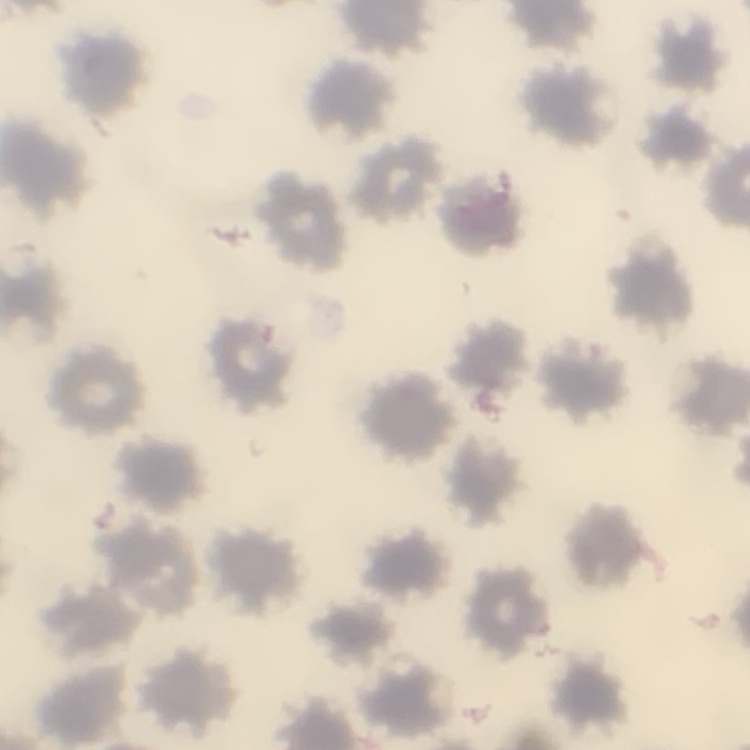
Summary:
  - Erythrocyte morphology: no rouleaux formation
  - Preparation: thin blood film
  - Image type: one tile cut from a larger photomicrograph
  - Stain: Field's or Giemsa